Identify the cell.
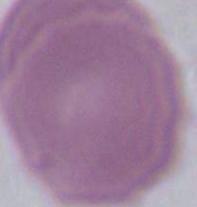
An erythrocyte.

Captured at 1000x magnification. Photomicrograph.